Assess this cell for malaria.
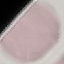

It is uninfected.

Giemsa-stained preparation. Acquired by smartphone through the microscope eyepiece. Automatically extracted cell patch, resized to 64 × 64 pixels. Thin smear of blood.